Outline each blood parasite and name the species.
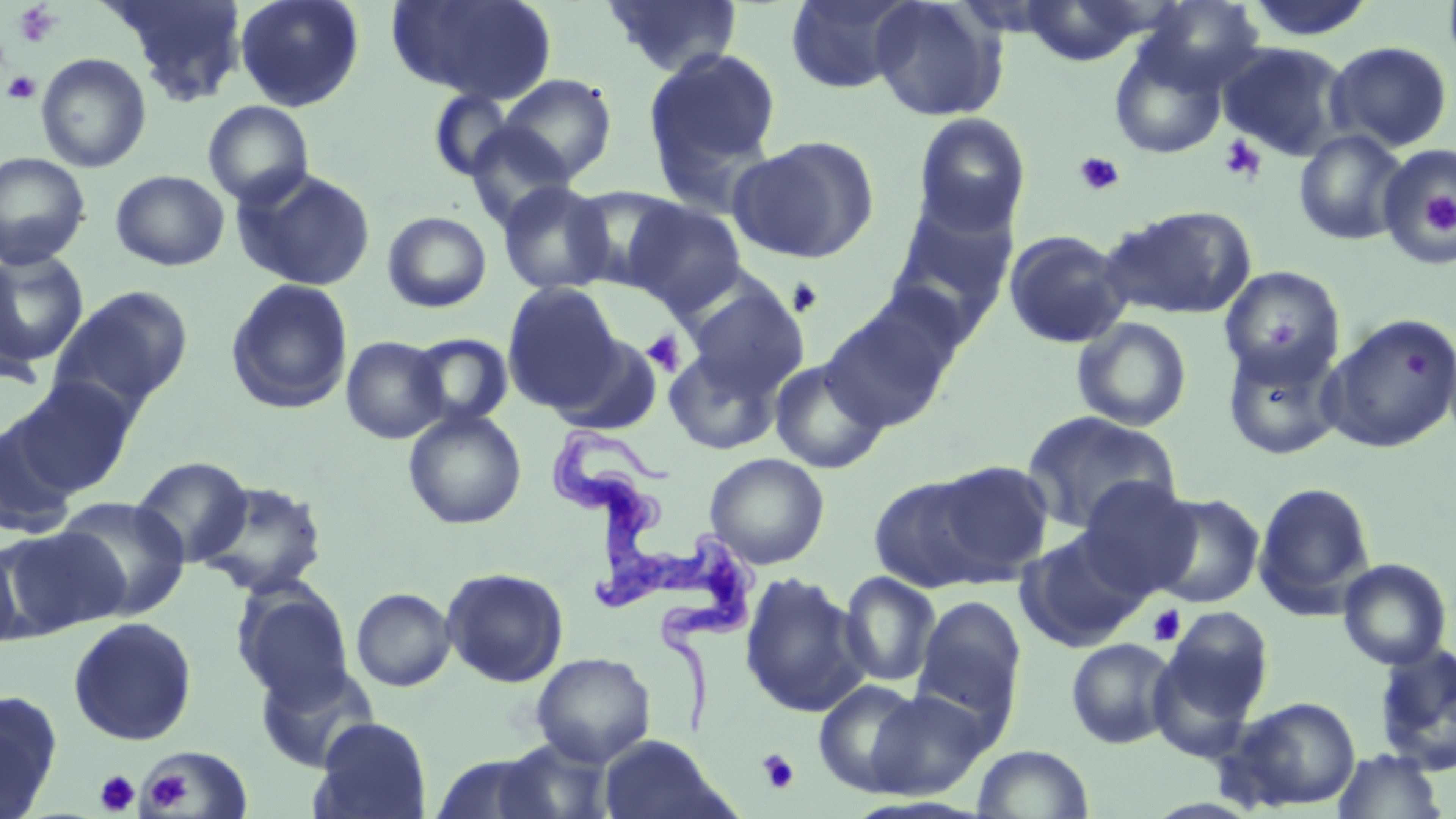
Approximate bounding boxes as (x1, y1, x2, y2) in pixels.
Trypanosoma brucei: (545, 426, 761, 740).
No Plasmodium falciparum, Plasmodium ovale, Plasmodium malariae, Plasmodium vivax, or Babesia divergens observed.

slide_level_diagnosis: Trypanosoma brucei
field_of_view: single
image_size: 1456×819 pixels
uninfected_red_blood_cell_locations: 'approximate bounding boxes as (x1, y1, x2, y2) in pixels: (106, 0, 249, 101), (234, 0, 365, 112), (386, 0, 558, 104), (604, 0, 743, 78), (784, 0, 918, 93), (870, 0, 1008, 122), (1141, 0, 1267, 94), (1017, 2, 1156, 66), (1109, 38, 1228, 159), (1326, 41, 1454, 152), (1216, 42, 1349, 161), (643, 45, 782, 191), (36, 52, 152, 173), (497, 73, 618, 182), (427, 89, 519, 181), (202, 101, 314, 209), (912, 112, 1032, 236), (464, 123, 576, 229), (1293, 130, 1408, 245), (729, 135, 880, 264), (1379, 142, 1456, 264), (0, 152, 91, 270), (235, 168, 376, 291), (110, 169, 230, 271), (498, 181, 614, 296), (566, 185, 690, 291), (884, 198, 1018, 329), (623, 200, 747, 315), (1101, 205, 1257, 320), (382, 211, 492, 313), (1003, 229, 1132, 348), (0, 249, 89, 370), (1219, 265, 1345, 384), (225, 278, 354, 415), (502, 281, 623, 411), (50, 285, 194, 416), (684, 285, 809, 397), (822, 304, 957, 432), (1323, 314, 1456, 454), (1072, 317, 1192, 432), (408, 333, 514, 429), (549, 333, 664, 435), (341, 336, 449, 444), (1221, 341, 1344, 461), (663, 347, 781, 455), (769, 357, 889, 474), (14, 377, 139, 495), (403, 408, 527, 530), (1021, 411, 1182, 533), (0, 418, 80, 539), (704, 452, 829, 570), (131, 456, 253, 567), (930, 460, 1055, 579), (868, 473, 1002, 594), (1076, 477, 1200, 598), (197, 480, 329, 599), (1253, 481, 1377, 617), (1147, 492, 1264, 608), (56, 496, 191, 619), (1, 526, 128, 636), (1017, 530, 1150, 651), (0, 539, 25, 654), (1337, 558, 1452, 670), (441, 567, 569, 688), (739, 572, 869, 718), (840, 572, 940, 687), (233, 583, 355, 705), (351, 587, 455, 692), (912, 595, 1026, 731), (1160, 606, 1274, 727), (68, 616, 197, 746), (1066, 638, 1178, 749), (1373, 642, 1456, 777), (532, 652, 656, 767), (256, 662, 379, 773), (813, 679, 927, 795), (864, 689, 991, 798), (0, 691, 63, 817), (1221, 695, 1361, 812), (311, 717, 432, 819), (599, 735, 730, 818), (486, 738, 620, 819), (972, 744, 1094, 818), (143, 748, 252, 817), (1330, 749, 1449, 819), (428, 754, 568, 818)'
magnification: 1000x
preparation: thin blood film
modality: optical microscopy
platelet_locations: 'approximate bounding boxes as (x1, y1, x2, y2) in pixels: (12, 3, 61, 49), (2, 70, 42, 105), (1218, 135, 1267, 184), (1073, 150, 1126, 197), (1424, 190, 1456, 234), (787, 277, 824, 317), (642, 330, 686, 376), (1147, 605, 1185, 646), (757, 749, 799, 794), (146, 768, 192, 810), (95, 769, 140, 815)'
stain: May-Grünwald-Giemsa